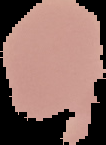
image size = 106×145 pixels
malaria status = uninfected
preparation = thin blood film
image type = segmented cell region with the area outside set to black